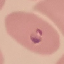 Malaria status: parasitized. Photographed with a smartphone camera at the microscope eyepiece. Giemsa-stained preparation. Thin blood film. Automatically extracted cell patch, resized to 64 × 64 pixels.